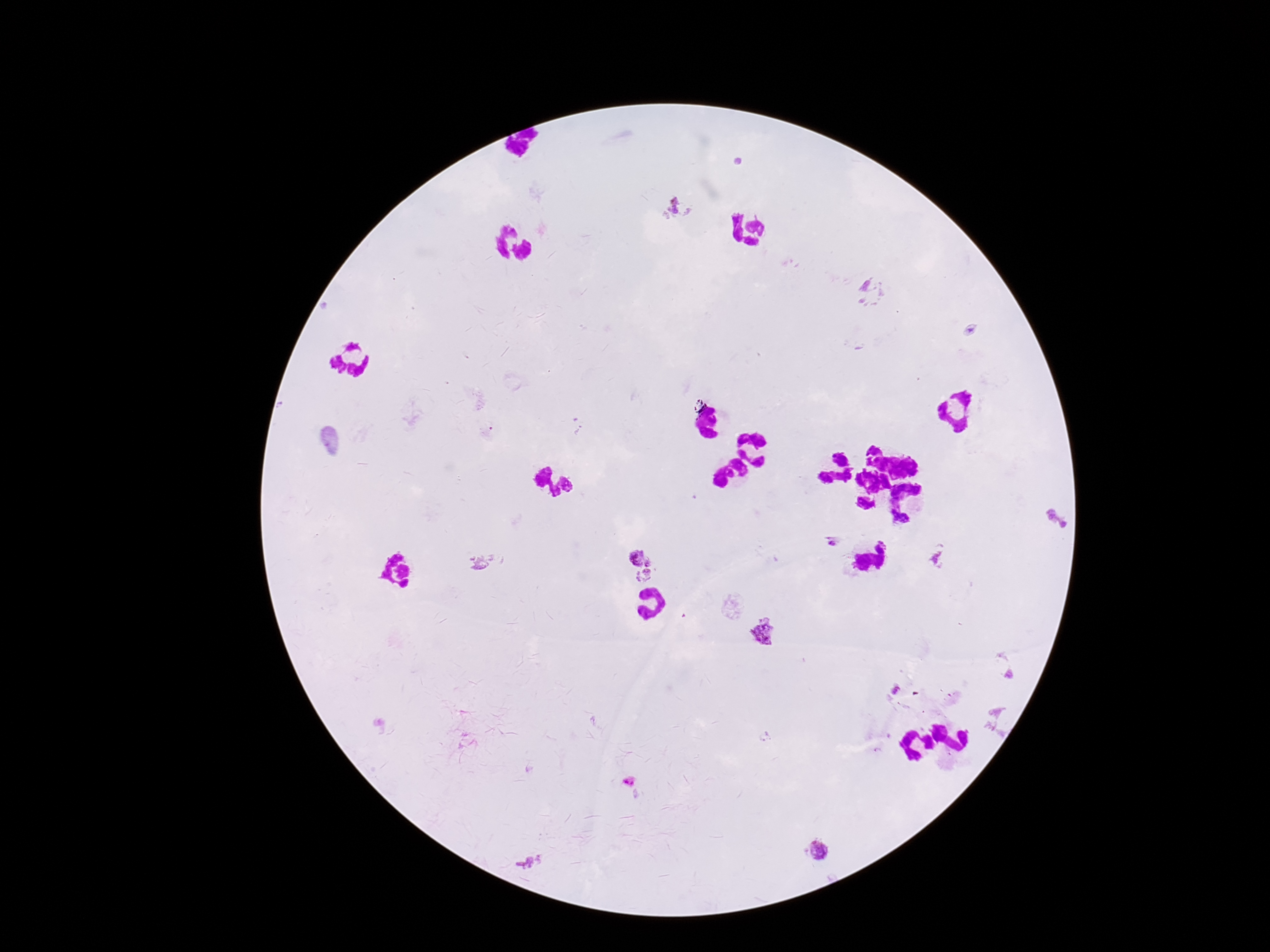
Approximate centers as (x, y) in pixels.
Summary:
  - Plasmodium parasite locations: (678, 209), (874, 292), (1059, 517), (831, 541), (940, 558), (488, 563), (640, 566), (767, 634), (819, 852), (527, 864)
  - Capture: smartphone camera through the microscope eyepiece
  - Field of view: one from this slide
  - Preparation: thick peripheral-blood smear
  - Patient malaria status: positive
  - Magnification: 100x
  - Stain: Giemsa
  - Image size: 1270×952 pixels